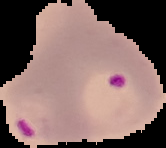
{
  "image_size": "166×148 pixels",
  "malaria_status": "parasitized",
  "preparation": "thin blood film",
  "image_type": "cell region segmented out of the field of view; surrounding area masked to black"
}